State which parasite is depicted.
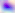
Toxoplasma gondii.

400x magnification. Photomicrograph.